Assess this cell for malaria.
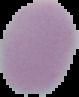

Uninfected.

Summary:
  - Preparation: thin blood smear
  - Image size: 79×97 pixels
  - Image type: segmented cell region on a black background